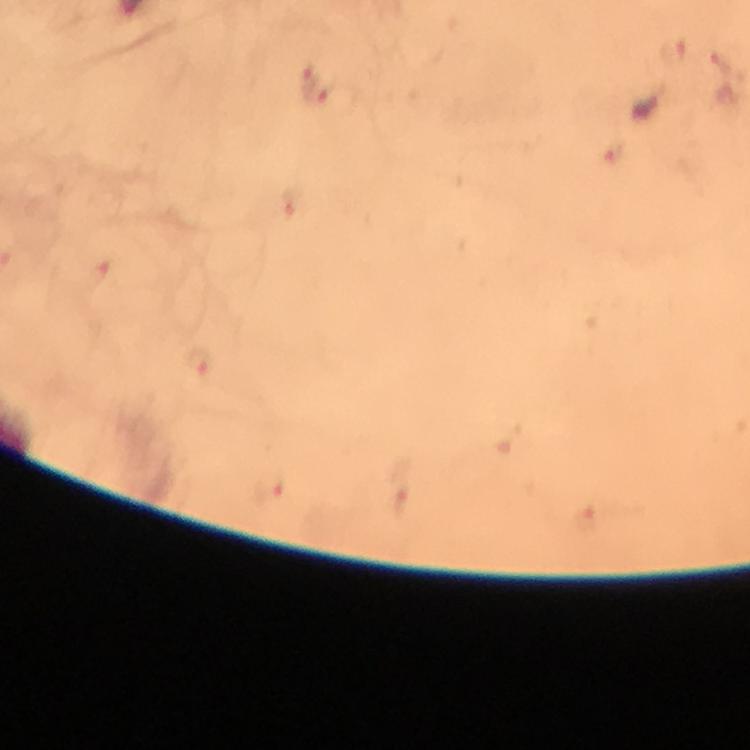 Approximate centers as (x, y) in pixels. Plasmodium parasite locations: (647, 109). Thick smear. A crop from one field of view. Immersion oil applied. Image is 750×750 pixels. From a malaria diagnostic workup. At 100x magnification. Giemsa-stained preparation. Photographed with a smartphone mounted on the microscope.